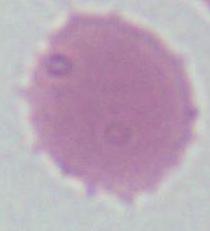
Summary:
  - Magnification: 1000x
  - Identification: red blood cell
  - Modality: photomicrograph